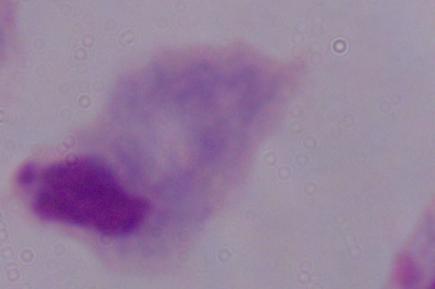

Summary:
  - Modality: micrograph
  - Identification: trichomonad
  - Magnification: 1000x